Comment on the morphology of the erythrocytes.
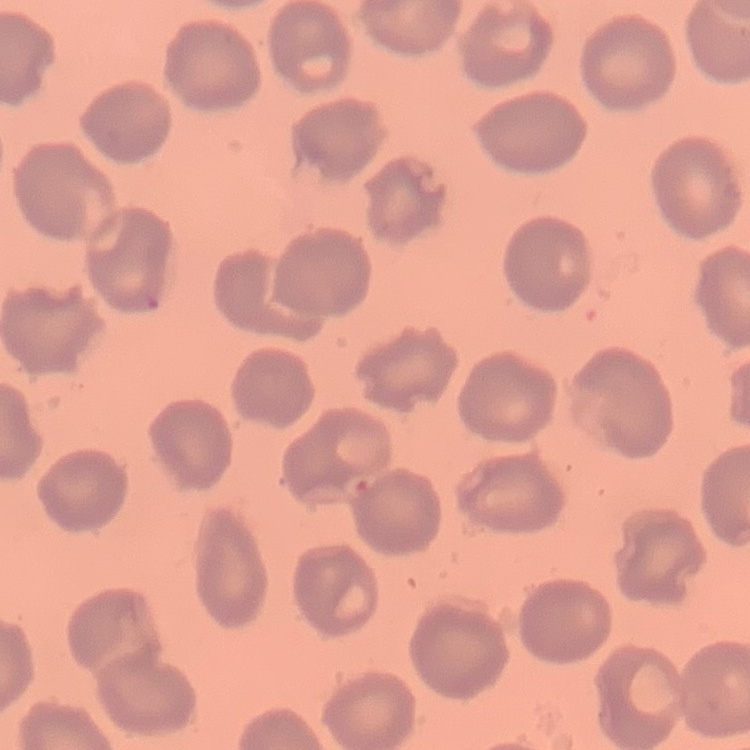

They show no rouleaux formation.

Thin blood smear. Square crop of a larger photomicrograph. Field's or Giemsa stain.